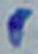
Summary:
  - Modality: photomicrograph
  - Identification: Toxoplasma gondii
  - Magnification: 1000x